Name the parasite shown.
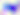

Toxoplasma gondii.

400x magnification. Photomicrograph.